State the preparation type.
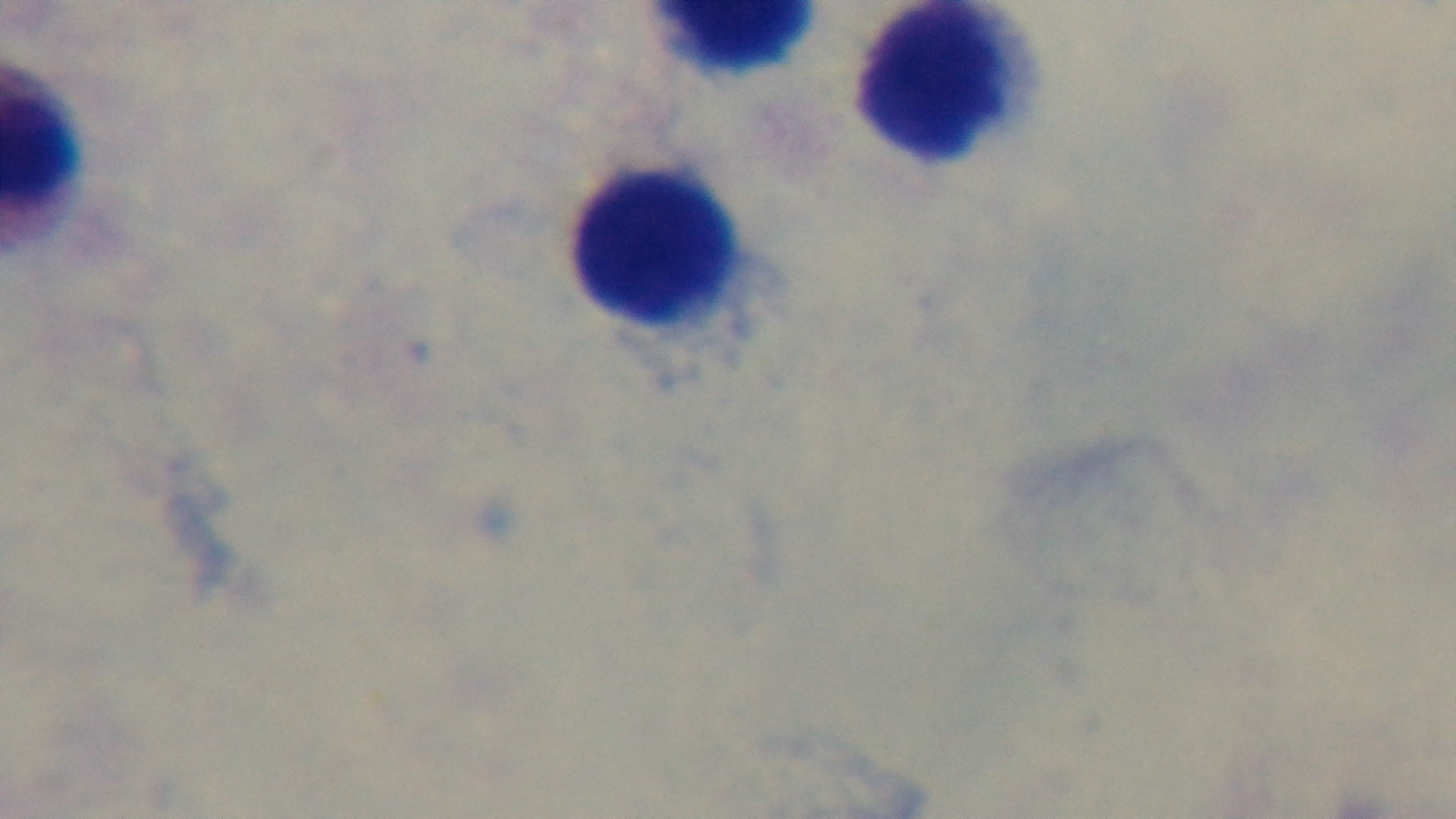
It is a thick blood film.

Malaria status: uninfected. One field from the slide. Photomicrograph. Oil-immersion objective, 100x. Giemsa stain. Mounted 4K digital camera.